Give the position of every Plasmodium parasite visible.
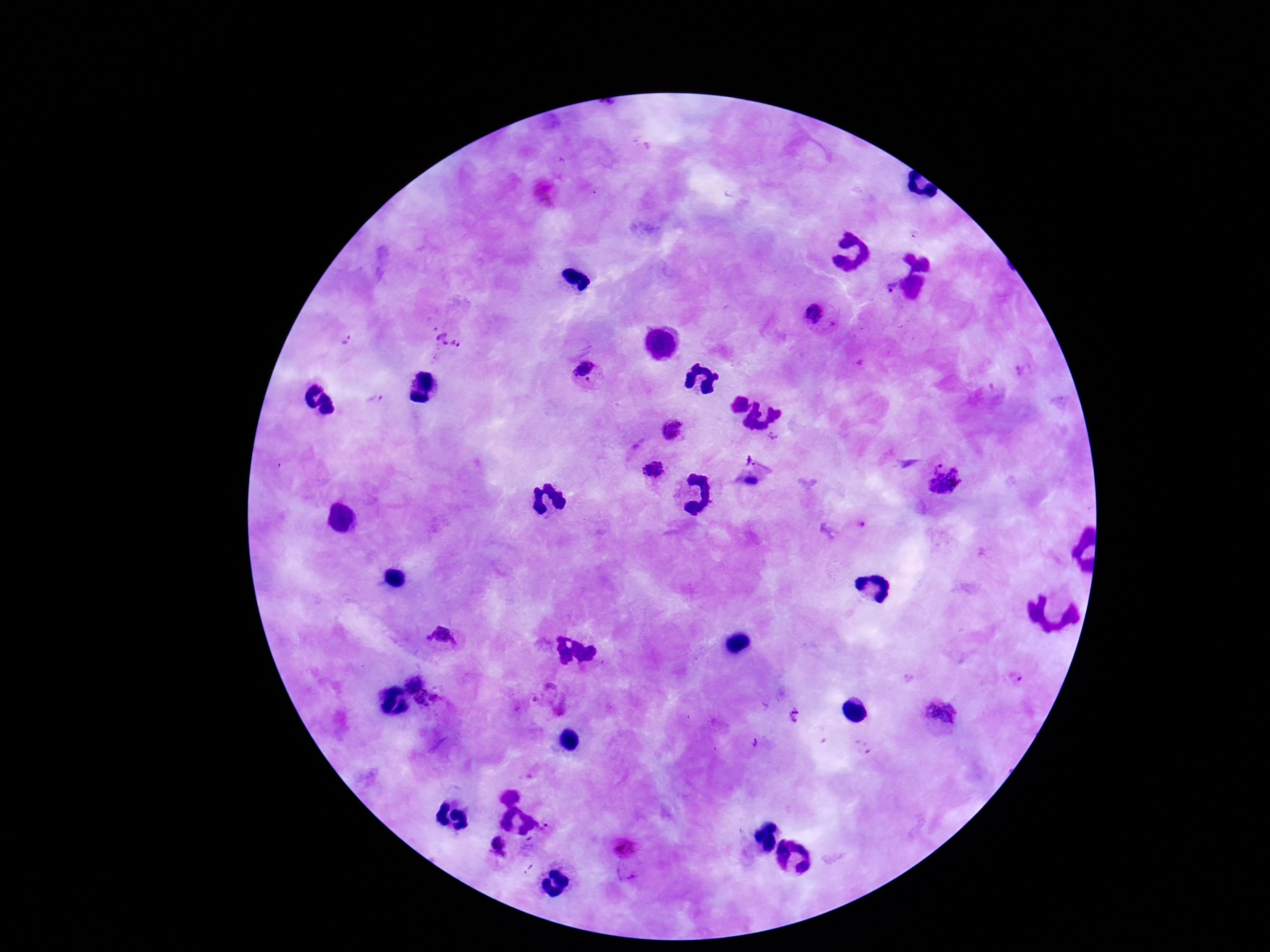

Approximate object centers, in pixels from the top-left corner.
Plasmodium parasites: (x=890, y=288), (x=812, y=314), (x=347, y=339), (x=448, y=340), (x=586, y=372), (x=374, y=399), (x=674, y=429), (x=774, y=435), (x=757, y=462), (x=935, y=466), (x=654, y=469), (x=750, y=481), (x=946, y=483), (x=846, y=532), (x=442, y=638), (x=1017, y=678), (x=414, y=681), (x=551, y=699), (x=428, y=701), (x=939, y=713), (x=794, y=717), (x=753, y=742), (x=506, y=788), (x=547, y=827), (x=527, y=845), (x=499, y=847), (x=623, y=849), (x=625, y=878).

Thick blood film. Smartphone photograph taken through the microscope eyepiece. Image is 1270×952 pixels. Patient malaria status: infected. Giemsa-stained preparation. 100x magnification. One field from this slide.